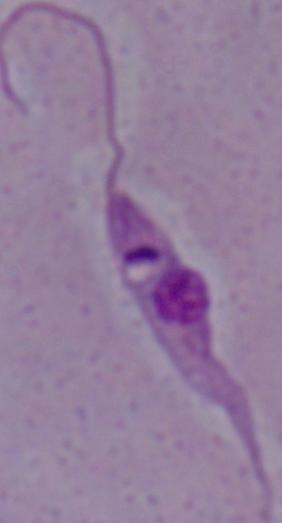
Summary:
  - Modality: photomicrograph
  - Identification: Leishmania
  - Magnification: 1000x